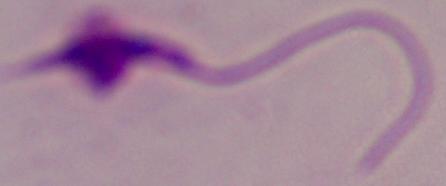
identification = Leishmania
modality = micrograph
magnification = 1000x